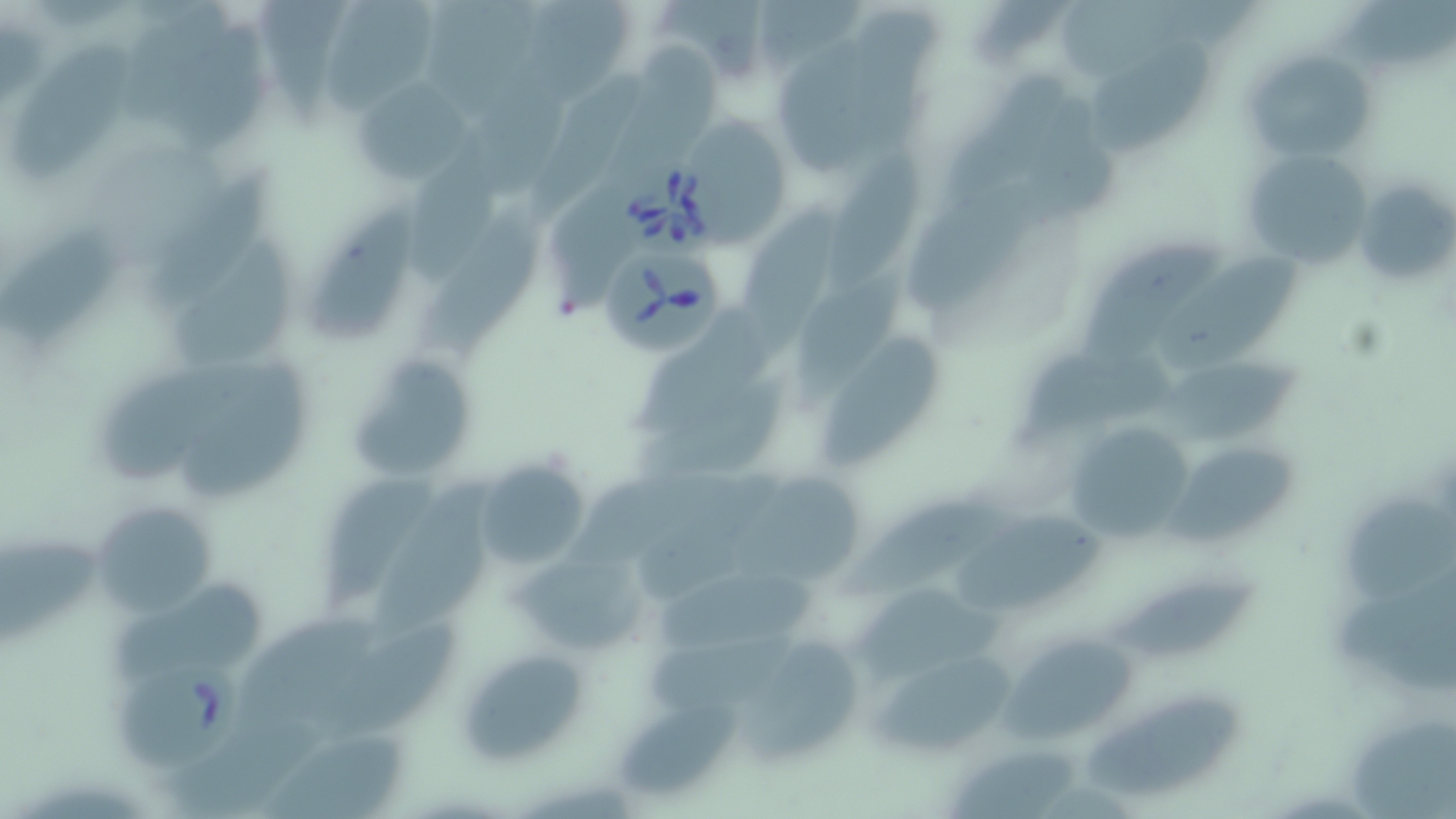
Summary:
  - Coordinate format: approximate bounding boxes as named x1/y1/x2/y2 corners in pixels
  - Babesia divergens-infected red blood cell locations: (x1=612, y1=151, x2=725, y2=265), (x1=603, y1=246, x2=724, y2=357), (x1=115, y1=657, x2=245, y2=772)
  - Uninfected red blood cell locations: (x1=533, y1=0, x2=630, y2=101), (x1=654, y1=0, x2=765, y2=77), (x1=757, y1=0, x2=868, y2=69), (x1=1356, y1=0, x2=1456, y2=61), (x1=120, y1=2, x2=229, y2=128), (x1=1060, y1=2, x2=1193, y2=81), (x1=431, y1=3, x2=534, y2=117), (x1=260, y1=4, x2=344, y2=121), (x1=338, y1=7, x2=437, y2=107), (x1=856, y1=10, x2=944, y2=154), (x1=171, y1=28, x2=269, y2=149), (x1=1084, y1=34, x2=1209, y2=159), (x1=778, y1=37, x2=882, y2=179), (x1=12, y1=39, x2=138, y2=183), (x1=614, y1=45, x2=731, y2=191), (x1=1240, y1=47, x2=1376, y2=165), (x1=476, y1=50, x2=576, y2=197), (x1=530, y1=62, x2=648, y2=217), (x1=948, y1=67, x2=1067, y2=204), (x1=354, y1=74, x2=472, y2=187), (x1=1016, y1=90, x2=1121, y2=230), (x1=693, y1=117, x2=789, y2=243), (x1=1240, y1=147, x2=1374, y2=269), (x1=407, y1=148, x2=502, y2=286), (x1=823, y1=148, x2=933, y2=292), (x1=148, y1=171, x2=278, y2=320), (x1=1354, y1=177, x2=1455, y2=290), (x1=907, y1=180, x2=1037, y2=305), (x1=737, y1=199, x2=854, y2=357), (x1=420, y1=203, x2=541, y2=357), (x1=308, y1=206, x2=426, y2=339), (x1=4, y1=229, x2=117, y2=348), (x1=169, y1=235, x2=293, y2=370), (x1=1079, y1=240, x2=1221, y2=359), (x1=1160, y1=259, x2=1310, y2=369), (x1=793, y1=271, x2=907, y2=414), (x1=632, y1=308, x2=763, y2=441), (x1=820, y1=336, x2=948, y2=468), (x1=1022, y1=348, x2=1179, y2=449), (x1=350, y1=353, x2=480, y2=485), (x1=179, y1=356, x2=308, y2=495), (x1=1159, y1=361, x2=1310, y2=447), (x1=103, y1=367, x2=222, y2=486), (x1=629, y1=373, x2=794, y2=484), (x1=1064, y1=417, x2=1201, y2=545), (x1=1170, y1=450, x2=1301, y2=540), (x1=474, y1=460, x2=592, y2=571), (x1=571, y1=467, x2=719, y2=563), (x1=317, y1=472, x2=442, y2=615), (x1=726, y1=472, x2=861, y2=588), (x1=372, y1=480, x2=498, y2=644), (x1=839, y1=497, x2=1006, y2=600), (x1=93, y1=499, x2=220, y2=620), (x1=1354, y1=502, x2=1456, y2=598), (x1=959, y1=506, x2=1101, y2=613), (x1=3, y1=538, x2=100, y2=647), (x1=513, y1=547, x2=644, y2=656), (x1=660, y1=568, x2=823, y2=650), (x1=114, y1=576, x2=262, y2=676), (x1=1334, y1=576, x2=1456, y2=695), (x1=860, y1=579, x2=1005, y2=685), (x1=1116, y1=581, x2=1266, y2=656), (x1=242, y1=609, x2=389, y2=729), (x1=321, y1=621, x2=463, y2=742), (x1=648, y1=628, x2=802, y2=713), (x1=749, y1=631, x2=860, y2=760), (x1=988, y1=633, x2=1136, y2=744), (x1=459, y1=646, x2=592, y2=766), (x1=866, y1=647, x2=1021, y2=759), (x1=1085, y1=696, x2=1246, y2=795), (x1=624, y1=698, x2=742, y2=795), (x1=168, y1=716, x2=333, y2=819), (x1=1354, y1=726, x2=1455, y2=819), (x1=265, y1=728, x2=410, y2=819), (x1=946, y1=751, x2=1080, y2=819)
  - Slide-level diagnosis: Babesia divergens
  - Field of view: single
  - Magnification: 1000x
  - Stain: May-Grünwald-Giemsa
  - Image size: 1456×819 pixels
  - Preparation: thin blood film
  - Modality: optical microscopy